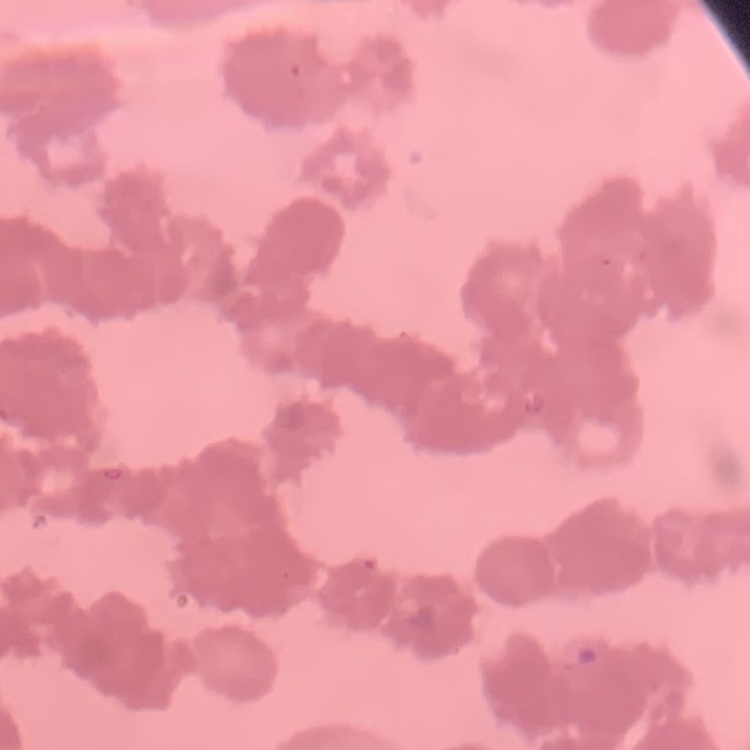

The erythrocytes show rouleaux formation. One tile cut from a larger photomicrograph. Thin blood film. Stained with either Field's or Giemsa.